Report the malaria status.
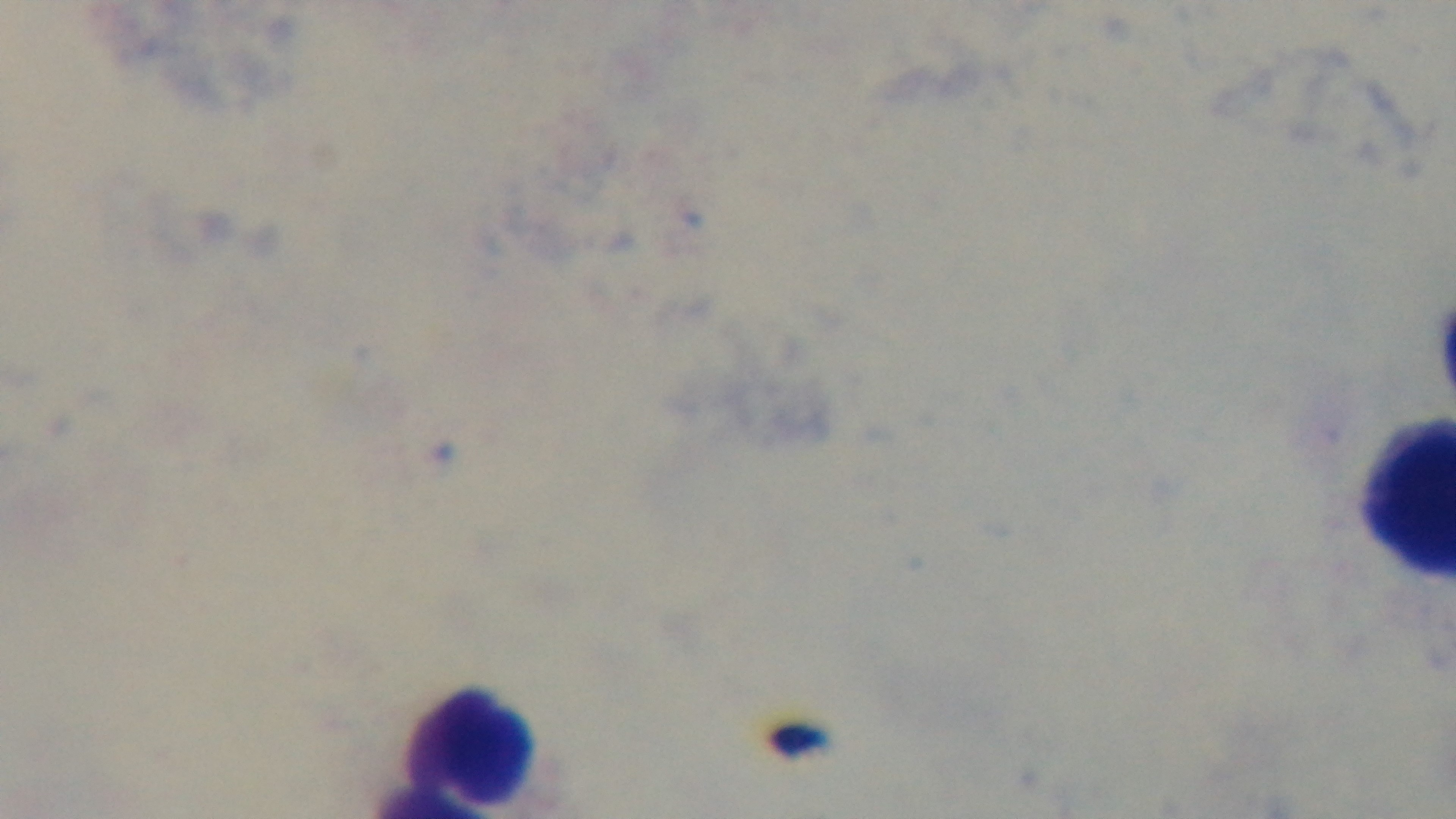

Negative.

objective = 100x oil immersion
preparation = thick blood film
capture = mounted 4K digital camera
modality = light microscopy
stain = Giemsa
field of view = single